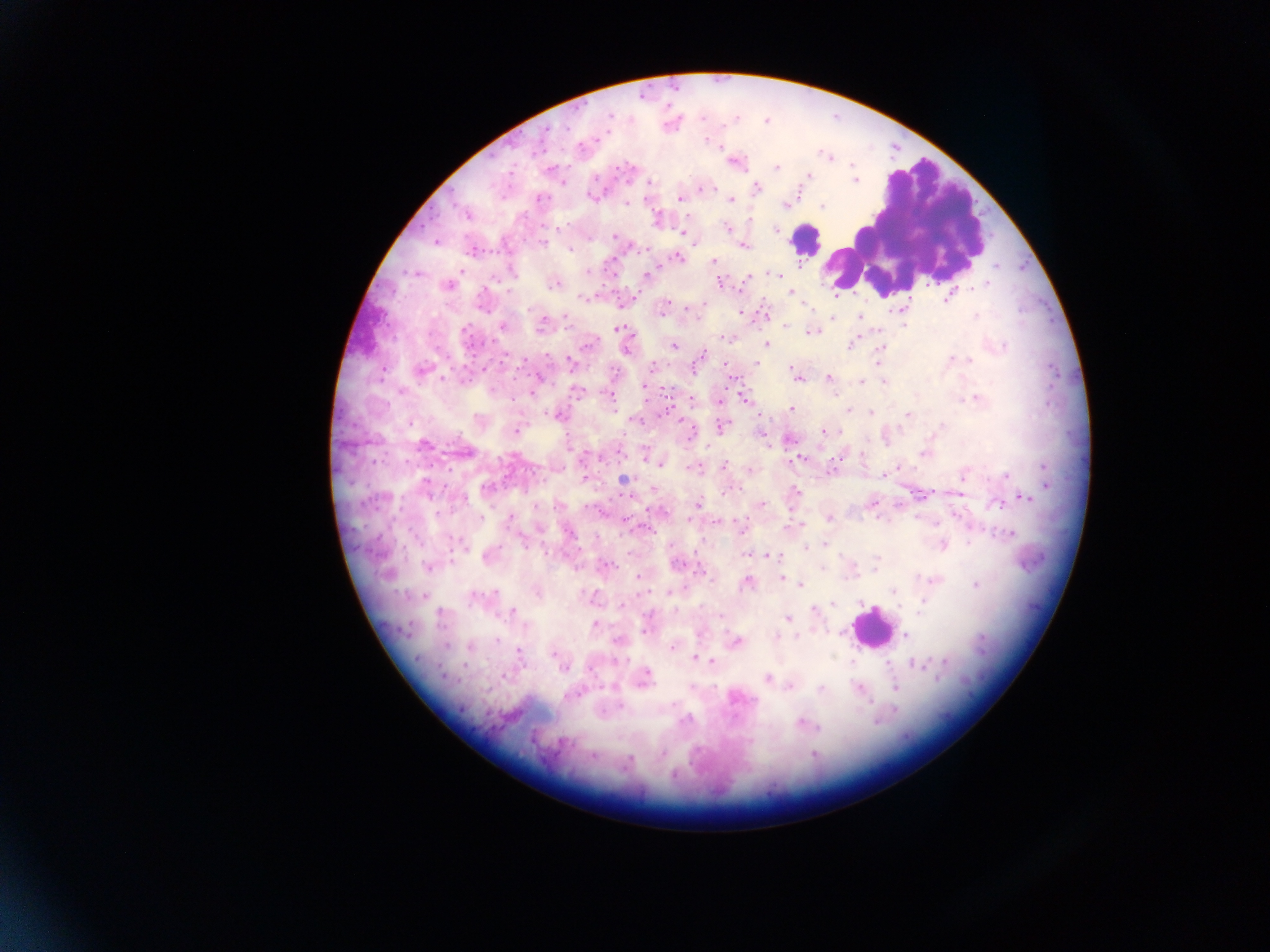
capture = mobile-phone photograph through a microscope
Plasmodium parasite locations = approximate centers as (x, y) in pixels: (609, 115), (702, 118), (735, 118), (568, 127), (546, 129), (602, 136), (705, 141), (717, 147), (827, 155), (852, 165), (776, 167), (619, 168), (808, 177), (854, 181), (563, 183), (649, 183), (712, 188), (706, 189), (757, 189), (592, 196), (539, 199), (680, 199), (732, 200), (626, 204), (784, 206), (822, 207), (467, 214), (748, 219), (657, 220), (562, 226), (727, 227), (775, 230), (682, 233), (615, 236), (436, 242), (542, 243), (745, 245), (570, 249), (473, 250), (678, 258), (713, 261), (996, 266), (799, 267), (462, 271), (588, 272), (414, 274), (646, 275), (778, 275), (784, 275), (748, 277), (719, 282), (555, 284), (987, 284), (448, 286), (790, 291), (583, 298), (947, 299), (703, 304), (665, 305), (688, 307), (740, 312), (765, 313), (976, 316), (860, 317), (698, 318), (832, 318), (566, 319), (544, 321), (903, 325), (502, 326), (542, 327), (785, 327), (618, 329), (465, 330), (879, 331), (808, 333), (724, 338), (588, 344), (767, 344), (673, 346), (850, 347), (882, 347), (1005, 347), (626, 350), (701, 354), (951, 359), (969, 360), (569, 361), (877, 362), (757, 363), (725, 365), (652, 366), (695, 368), (790, 368), (420, 370), (539, 378), (829, 378), (443, 379), (797, 379), (861, 381), (885, 382), (645, 388), (493, 390), (665, 391), (401, 392), (532, 392), (577, 392), (611, 397), (976, 397), (692, 399), (720, 400), (745, 400), (792, 409), (847, 411), (871, 413), (908, 414), (556, 415), (636, 421), (684, 425), (941, 425), (722, 426), (516, 430), (823, 431), (839, 431), (689, 436), (790, 439), (424, 445), (766, 445), (461, 451), (923, 454), (862, 455), (585, 456), (647, 458), (799, 458), (659, 464), (724, 466), (1045, 466), (901, 468), (695, 469), (749, 469), (883, 476), (1006, 476), (963, 478), (624, 479), (426, 484), (1047, 485), (486, 487), (654, 489), (737, 489), (796, 491), (726, 493), (1025, 498), (464, 499), (697, 503), (762, 504), (997, 505), (537, 506), (957, 515), (830, 517), (481, 518), (510, 518), (917, 518), (689, 519), (717, 523), (801, 523), (741, 528), (570, 534), (1010, 534), (968, 543), (458, 544), (824, 545), (942, 545), (806, 548), (547, 554), (745, 555), (768, 555), (487, 557), (877, 557), (607, 565), (677, 565), (427, 566), (822, 569), (875, 570), (702, 571), (637, 577), (781, 577), (917, 577), (935, 580), (748, 583), (800, 585), (974, 585), (536, 591), (893, 591), (493, 593), (669, 593), (473, 596), (424, 597), (923, 600), (861, 602), (832, 603), (623, 604), (814, 609), (513, 612), (440, 613), (649, 613), (721, 617), (787, 619), (595, 625), (646, 631), (775, 636), (906, 636), (796, 637), (496, 640), (617, 641), (736, 641), (446, 646), (470, 647), (672, 648), (519, 651), (553, 654), (695, 657), (711, 660), (944, 661), (852, 663), (886, 663), (916, 665), (464, 666), (564, 668), (590, 668), (646, 674), (504, 676), (644, 678), (767, 678), (789, 686), (859, 687), (895, 688), (820, 689), (672, 704), (621, 706), (683, 721), (877, 721), (800, 723), (819, 727), (662, 754), (814, 754), (593, 756), (630, 759), (674, 775)
preparation = thick blood film
country = Ghana
field of view = single
leukocyte locations = approximate centers as (x, y) in pixels: (904, 224), (806, 240), (871, 628)
image size = 1270×952 pixels